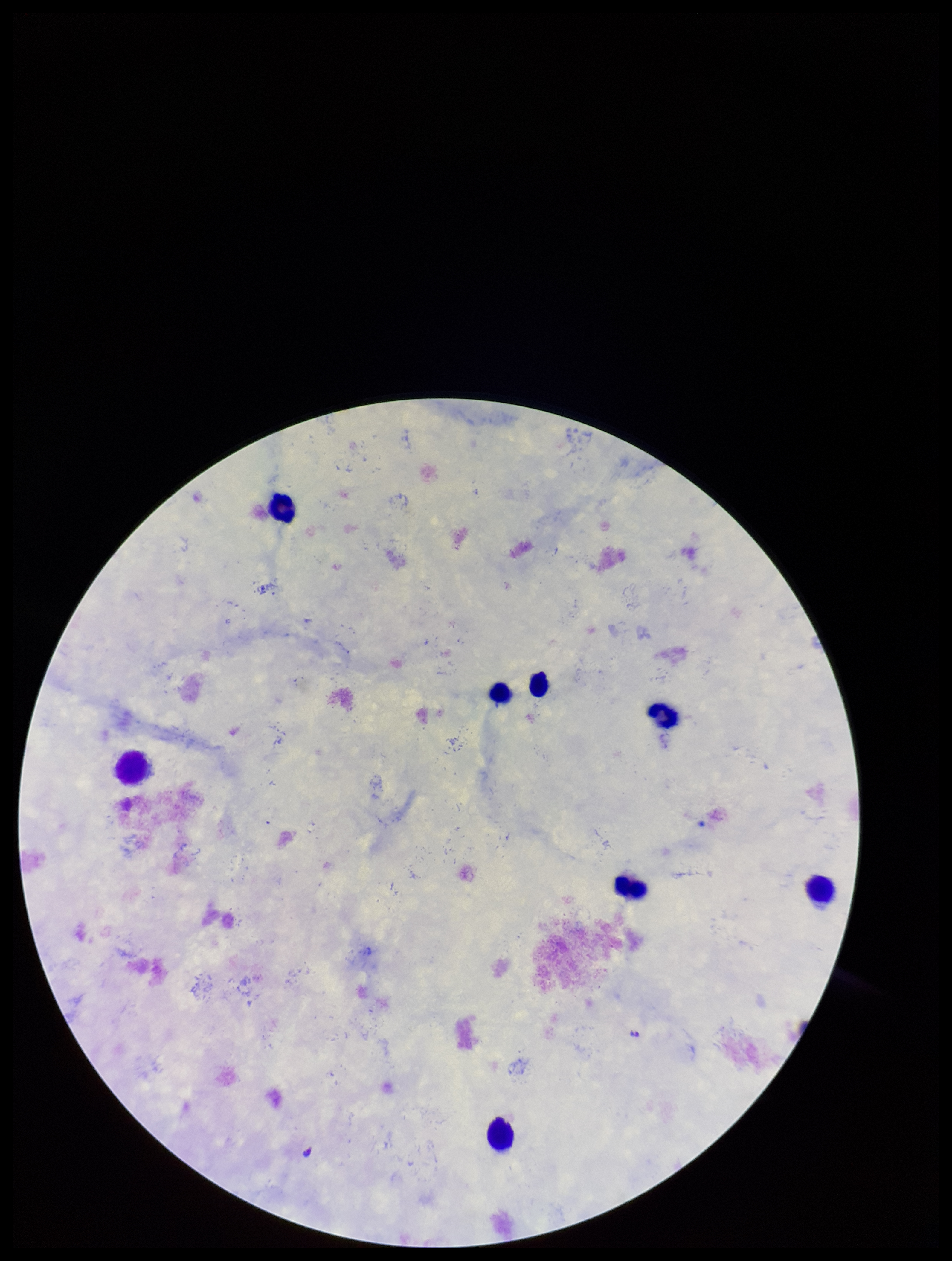

Preparation: thick smear. Plasmodium parasites: none identified. Species reported for this patient: Plasmodium falciparum. Parasite count: 0. Giemsa stain. Smartphone photograph taken through the eyepiece of a microscope. One field from this slide. Image is 952×1261 pixels. Patient malaria status: infected. Leukocyte count: 8.